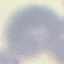

{
  "result": "no malaria parasites detected",
  "stain": "Giemsa",
  "capture": "smartphone through the microscope eyepiece",
  "preparation": "thin smear",
  "image_type": "automatically extracted cell patch, resized to 64 × 64 pixels"
}